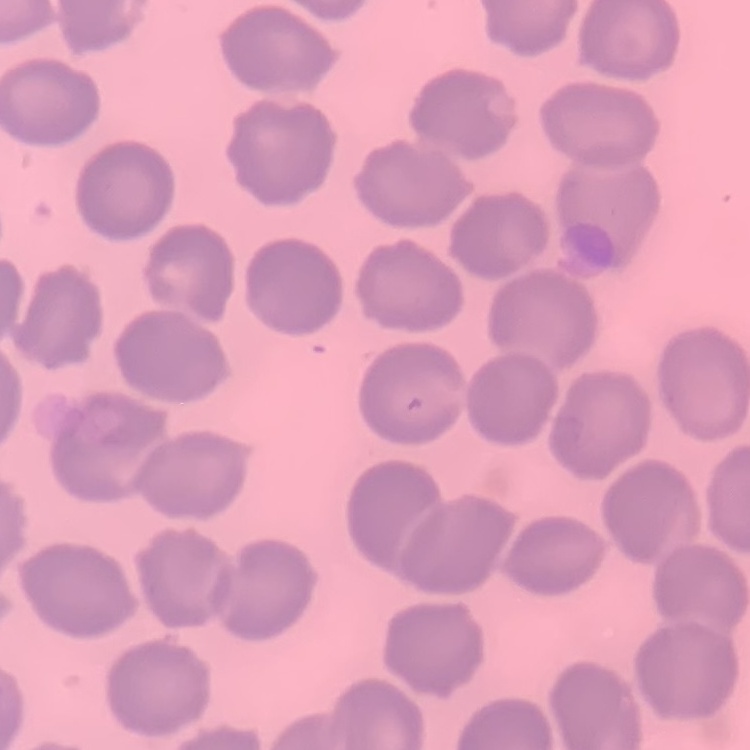

The erythrocytes show no rouleaux formation. Square crop of a larger photomicrograph. Field's or Giemsa stain. Thin blood smear.